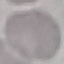
Summary:
  - Malaria status: uninfected
  - Stain: Giemsa
  - Capture: smartphone through the microscope eyepiece
  - Preparation: thin blood film
  - Image type: automatically extracted cell patch, resized to 64 × 64 pixels